Outline each blood parasite and name the species.
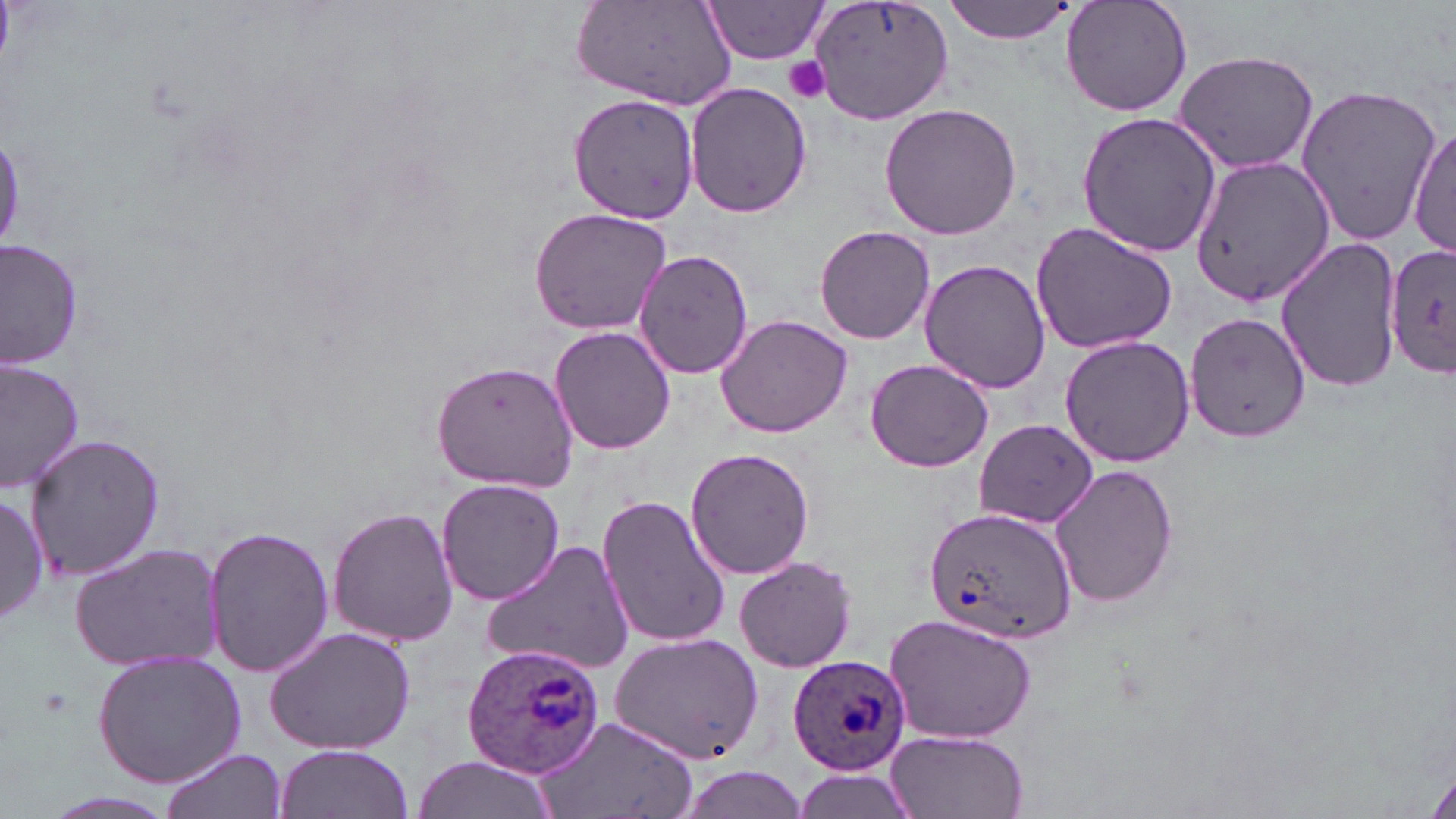

Approximate bounding boxes as (x1,y1)-(x2,y2) corner pairs in pixels.
Plasmodium ovale-infected red blood cells: (924,504)-(1077,647), (461,644)-(605,775), (788,655)-(912,775).
No Plasmodium falciparum, Plasmodium malariae, Plasmodium vivax, Babesia divergens, or Trypanosoma brucei observed.

Uninfected red blood cell locations: (576,0)-(739,112), (942,0)-(1076,43), (1062,0)-(1193,117), (702,1)-(834,66), (806,1)-(955,126), (1173,49)-(1320,171), (687,82)-(812,218), (1294,84)-(1441,245), (569,94)-(699,224), (880,103)-(1023,240), (1074,111)-(1223,258), (1410,124)-(1455,259), (1192,156)-(1336,307), (527,207)-(674,336), (1030,220)-(1177,354), (816,225)-(936,345), (1276,235)-(1401,394), (1,237)-(85,371), (1385,244)-(1456,379), (633,247)-(754,379), (920,259)-(1051,395), (1185,310)-(1312,442), (715,312)-(852,437), (549,324)-(675,455), (1058,335)-(1195,467), (2,355)-(85,492), (865,358)-(993,472), (430,359)-(580,493), (973,418)-(1098,528), (27,432)-(166,584), (684,447)-(816,580), (1050,462)-(1177,609), (435,477)-(564,607), (0,489)-(47,631), (598,493)-(734,649), (329,506)-(458,647), (201,521)-(332,679), (481,539)-(635,675), (68,541)-(226,674), (734,556)-(856,672), (882,611)-(1038,744), (264,624)-(414,756), (609,634)-(764,762), (91,649)-(248,787), (535,716)-(699,819), (881,730)-(1032,819), (274,745)-(413,819), (159,749)-(286,819), (412,752)-(554,819), (673,765)-(813,818), (790,769)-(920,819). Platelet locations: (784,57)-(833,103). Slide-level diagnosis: Plasmodium ovale. May-Grünwald-Giemsa stain. Image is 1456×819 pixels. Optical microscopy. Thin blood film. 1000x magnification. One field of a larger specimen.